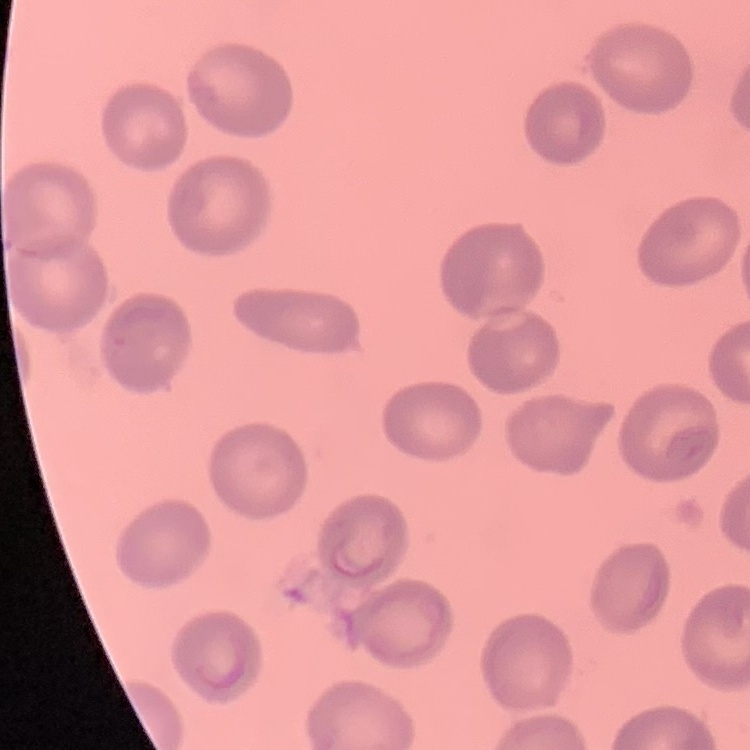
red blood cell morphology = no rouleaux formation
preparation = thin blood smear
image type = square crop of a larger photomicrograph
stain = Field's or Giemsa